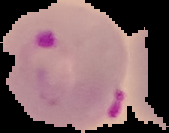

image_size: 169×133 pixels
image_type: segmented cell region on a black background
result: malaria parasites identified
preparation: thin blood film